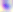
Summary:
  - Modality: micrograph
  - Magnification: 400x
  - Identification: Toxoplasma gondii